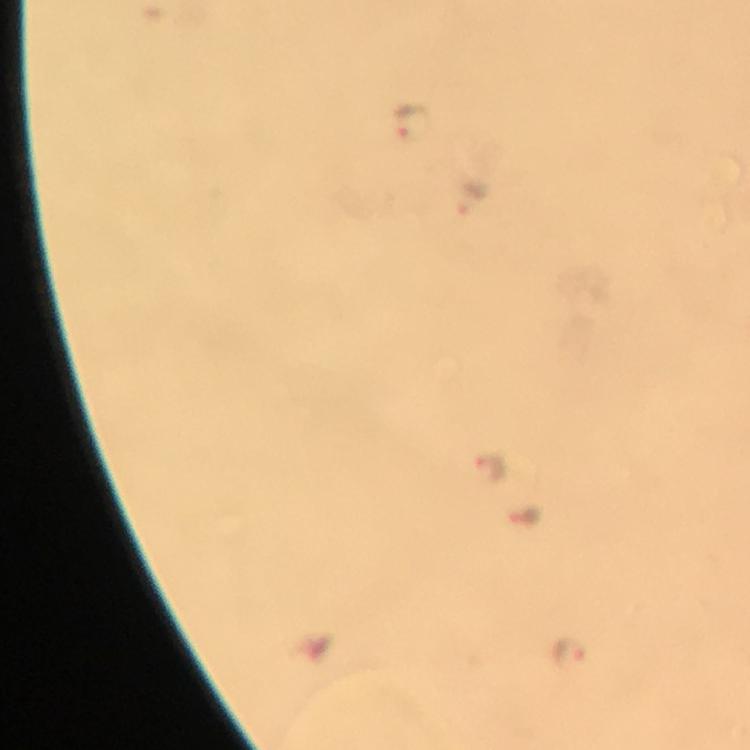
stain = Giemsa
image size = 750×750 pixels
malaria parasite locations = approximate centers as {x, y} in pixels: {412, 123}, {475, 199}, {493, 464}, {522, 513}, {569, 652}
immersion oil = used
preparation = thick blood smear
cropped from = a single field of view
context = from a malaria diagnostic workup
magnification = 100x
capture = smartphone camera through the microscope